Assess the morphology of the red blood cells.
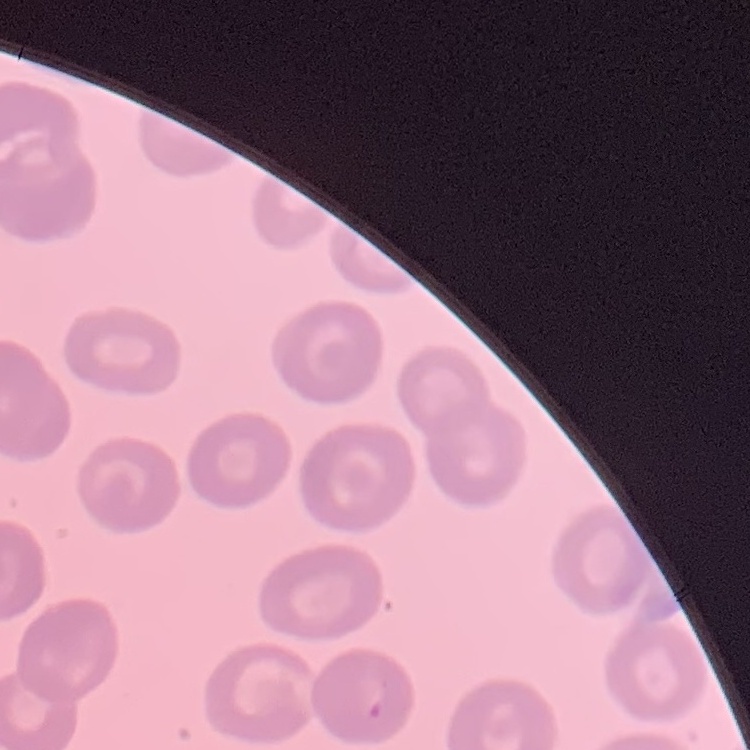

No rouleaux formation.

image_type: square crop of a larger photomicrograph
stain: Field's or Giemsa
preparation: thin peripheral smear